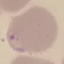
Malaria status: parasitized. Automatically extracted cell patch, resized to 64 × 64 pixels. Giemsa stain. Thin blood smear. Photographed with a smartphone camera at the microscope eyepiece.